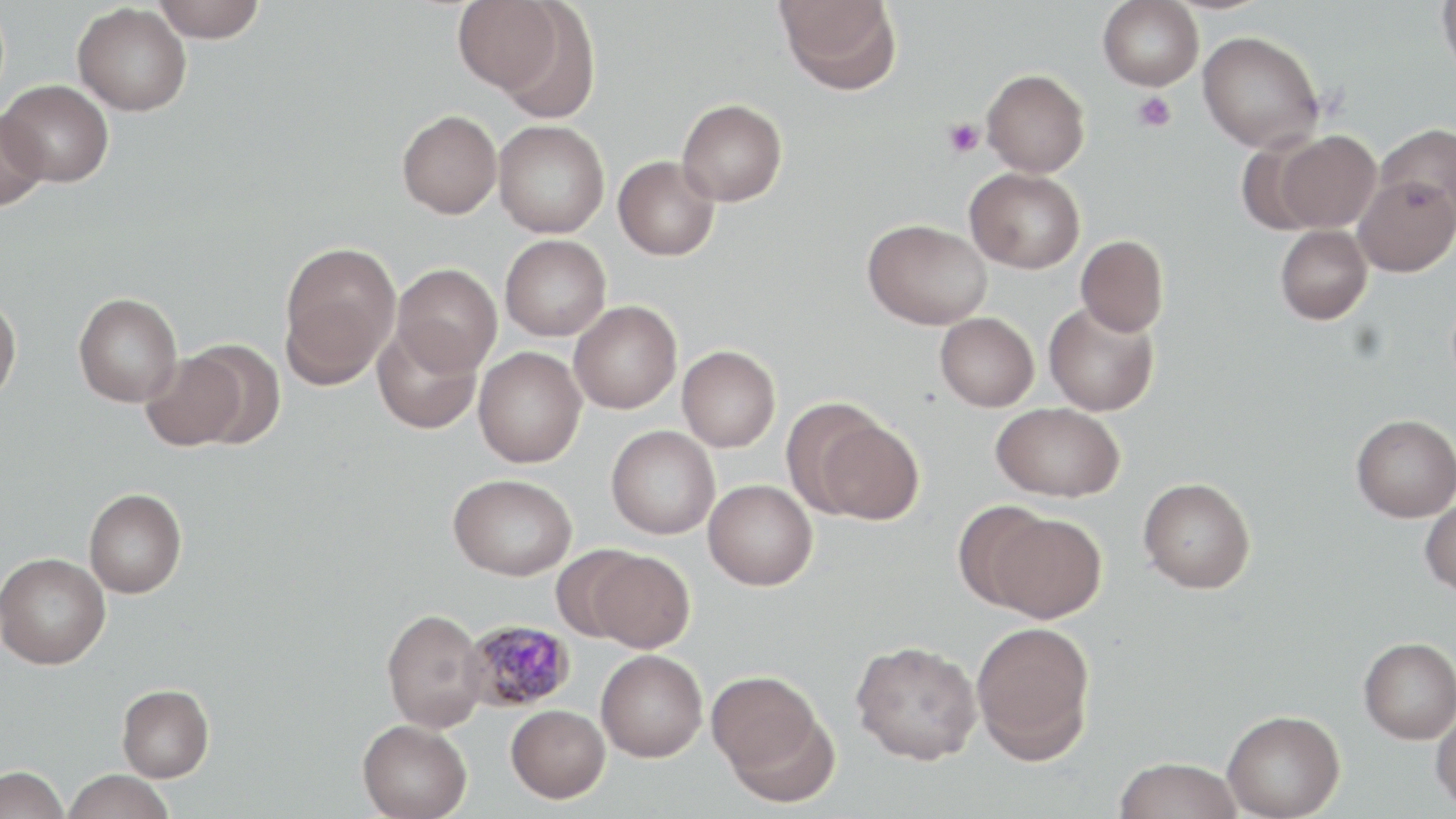 Approximate bounding boxes as (x1, y1, x2, y2) in pixels. Uninfected red blood cell locations: (152, 0, 266, 42), (453, 0, 565, 97), (776, 0, 901, 96), (1098, 0, 1203, 90), (1437, 0, 1456, 80), (73, 3, 191, 116), (1197, 30, 1325, 152), (982, 69, 1090, 177), (1, 79, 114, 187), (677, 99, 787, 206), (0, 107, 48, 210), (397, 109, 502, 218), (493, 119, 610, 238), (1375, 123, 1456, 222), (1274, 130, 1381, 233), (1235, 135, 1328, 236), (613, 155, 720, 261), (965, 167, 1085, 273), (1354, 174, 1456, 276), (863, 218, 992, 329), (1275, 224, 1372, 324), (500, 234, 611, 340), (1075, 235, 1169, 336), (278, 241, 401, 385), (392, 263, 502, 376), (73, 292, 183, 407), (0, 293, 22, 406), (569, 300, 682, 414), (1044, 300, 1160, 416), (935, 312, 1039, 411), (372, 325, 482, 434), (184, 341, 286, 449), (677, 345, 780, 452), (473, 347, 587, 468), (141, 349, 246, 451), (780, 398, 886, 517), (993, 402, 1124, 502), (1351, 414, 1456, 522), (812, 417, 925, 525), (606, 425, 720, 539), (449, 473, 577, 580), (1138, 477, 1256, 593), (703, 479, 818, 590), (84, 487, 187, 598), (1420, 496, 1456, 595), (953, 500, 1057, 610), (987, 511, 1107, 623), (550, 545, 649, 643), (587, 549, 694, 652), (0, 552, 110, 669), (382, 608, 488, 732), (970, 620, 1096, 764), (1359, 637, 1456, 744), (851, 640, 982, 764), (596, 649, 707, 761), (706, 669, 830, 793), (116, 684, 214, 782), (506, 704, 610, 802), (1431, 706, 1456, 814), (1223, 709, 1346, 819), (357, 719, 472, 819), (1115, 757, 1242, 819), (0, 765, 69, 819), (62, 769, 176, 819). Platelet locations: (1132, 91, 1177, 132), (943, 118, 985, 157). Plasmodium malariae-infected red blood cell locations: (461, 619, 577, 712). Slide-level diagnosis: Plasmodium malariae. Thin blood film. Single field of view. Light microscopy. 1000x magnification. Image is 1456×819 pixels. May-Grünwald-Giemsa stain.